Report the malaria status of this cell.
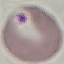
It is uninfected.

Giemsa stain. Cell patch, automatically extracted from a larger field of view and resized to 64 × 64 pixels. Acquired by smartphone through the microscope eyepiece. Thin blood smear.